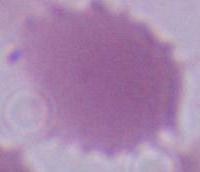

modality: micrograph
identification: red blood cell
magnification: 1000x